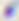

Toxoplasma gondii is seen. Micrograph. 400x magnification.